Name the parasite shown.
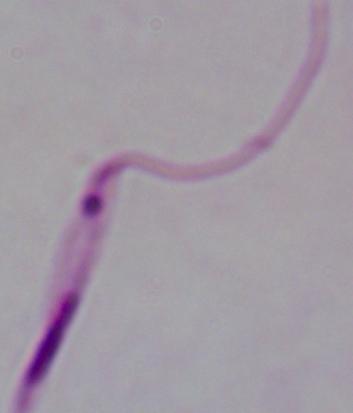
This is Leishmania.

Micrograph. 1000x magnification.